Name the parasite shown.
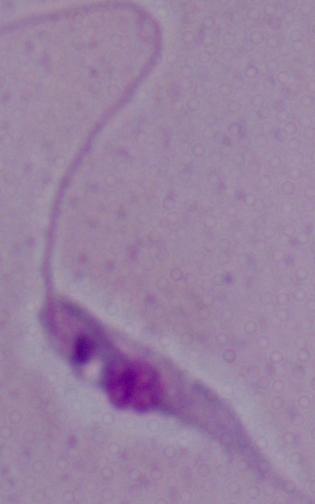

This is Leishmania.

magnification = 1000x
modality = photomicrograph